Report the malaria status of this cell.
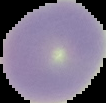

It is uninfected.

Cell region segmented out of the field of view; the surrounding area is masked to black. Image is 106×103 pixels. From a thin blood film.